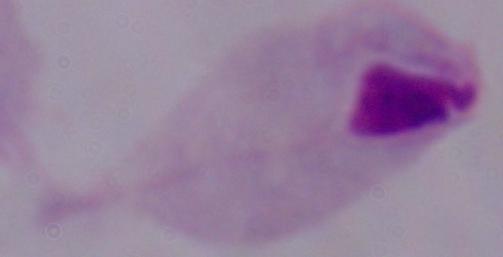
{
  "identification": "trichomonad",
  "modality": "micrograph",
  "magnification": "1000x"
}